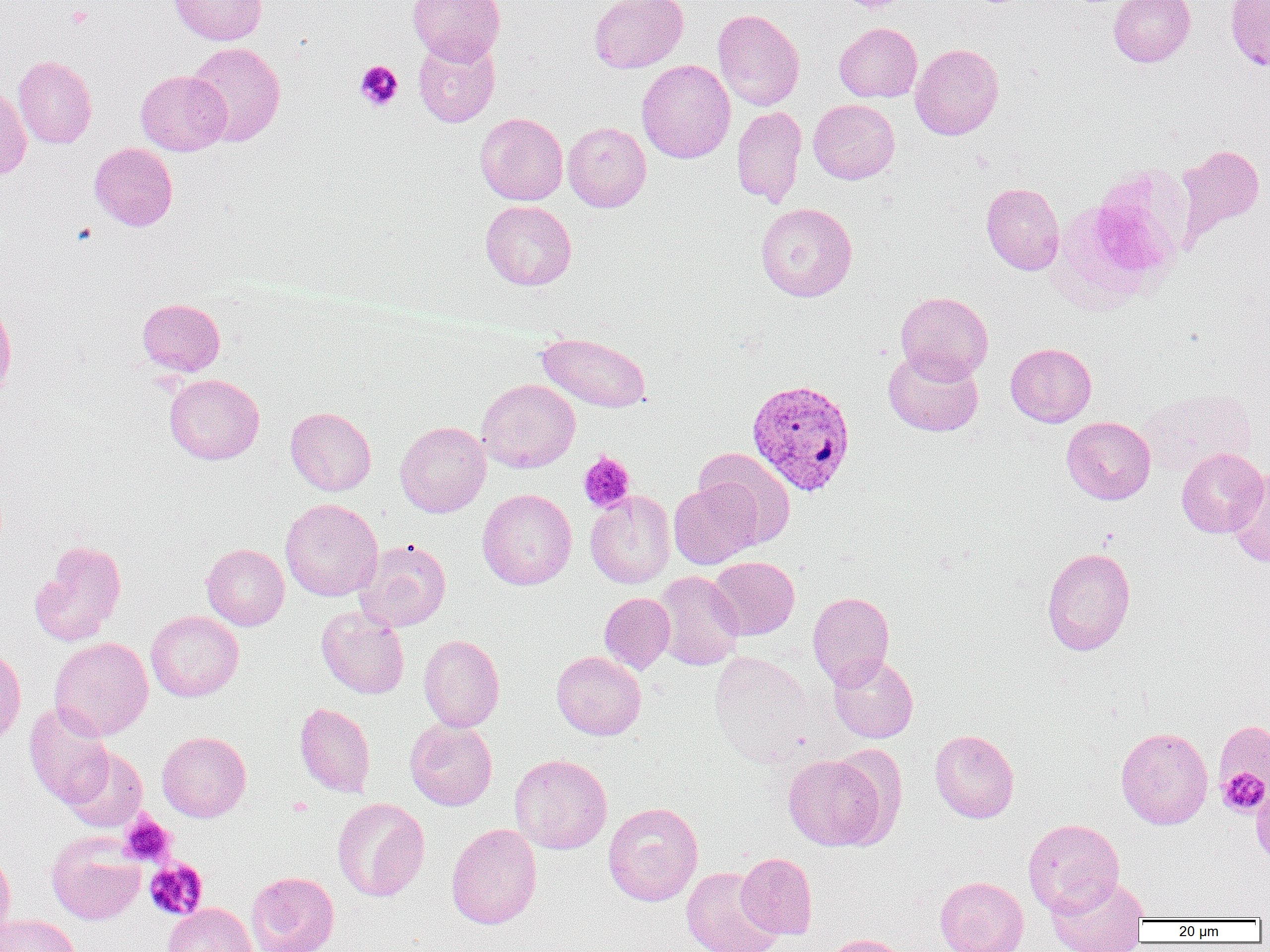

Summary:
  - Coordinate format: approximate bounding boxes as [x1, y1, x2, y2] in pixels
  - Uninfected red blood cell locations: [169, 0, 267, 44], [407, 0, 505, 64], [589, 0, 688, 73], [1109, 0, 1196, 67], [1225, 0, 1270, 70], [712, 9, 804, 110], [834, 22, 922, 102], [413, 36, 500, 127], [187, 42, 286, 147], [911, 43, 1004, 140], [13, 55, 97, 149], [636, 60, 735, 164], [136, 70, 231, 155], [0, 87, 31, 180], [808, 99, 900, 184], [731, 106, 806, 207], [475, 113, 568, 205], [563, 122, 651, 212], [89, 143, 178, 231], [1176, 144, 1265, 244], [981, 182, 1064, 275], [480, 200, 577, 290], [755, 202, 857, 302], [895, 291, 993, 383], [0, 298, 17, 402], [137, 298, 225, 375], [537, 332, 651, 413], [1006, 343, 1096, 427], [883, 349, 983, 437], [164, 374, 264, 464], [477, 378, 580, 473], [1139, 388, 1257, 476], [286, 406, 376, 496], [1062, 416, 1156, 504], [394, 421, 491, 517], [693, 448, 796, 548], [1176, 448, 1268, 537], [1227, 468, 1270, 568], [669, 480, 762, 569], [477, 488, 577, 590], [585, 491, 675, 588], [280, 498, 383, 601], [355, 539, 451, 631], [29, 540, 126, 646], [201, 543, 289, 631], [1042, 547, 1136, 655], [708, 556, 799, 640], [653, 571, 744, 670], [807, 591, 894, 688], [599, 592, 675, 673], [316, 606, 409, 699], [146, 611, 244, 702], [418, 634, 504, 732], [49, 637, 153, 741], [0, 643, 26, 747], [551, 651, 646, 740], [709, 651, 813, 766], [828, 653, 918, 744], [294, 702, 376, 798], [24, 703, 115, 808], [405, 718, 497, 810], [1215, 722, 1269, 803], [1115, 726, 1213, 829], [930, 729, 1019, 823], [157, 731, 251, 821], [62, 746, 148, 833], [510, 754, 612, 854], [783, 754, 887, 850], [1251, 778, 1270, 863], [332, 797, 430, 901], [603, 801, 703, 906], [1023, 818, 1124, 916], [446, 823, 541, 929], [46, 831, 145, 925], [0, 845, 15, 942], [735, 852, 818, 940], [142, 858, 220, 928], [681, 866, 781, 952], [246, 871, 339, 952], [1047, 875, 1149, 952], [935, 876, 1028, 952], [162, 903, 257, 952], [1, 914, 81, 952], [819, 934, 909, 952]
  - Platelet locations: [842, 0, 904, 13], [355, 60, 403, 110], [578, 451, 636, 513], [1217, 767, 1269, 816], [120, 813, 174, 867], [144, 858, 208, 920]
  - Plasmodium vivax-infected red blood cell locations: [746, 378, 856, 497]
  - Slide-level diagnosis: Plasmodium vivax
  - Preparation: thin blood smear
  - Field of view: single
  - Modality: light microscopy
  - Image size: 1270×952 pixels
  - Magnification: 1000x